Assess this cell for malaria.
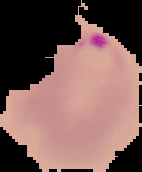
It is parasitized.

From a thin blood film. The area outside the segmented cell region is set to black. Image is 142×172 pixels.